Locate every malaria parasite and every leukocyte.
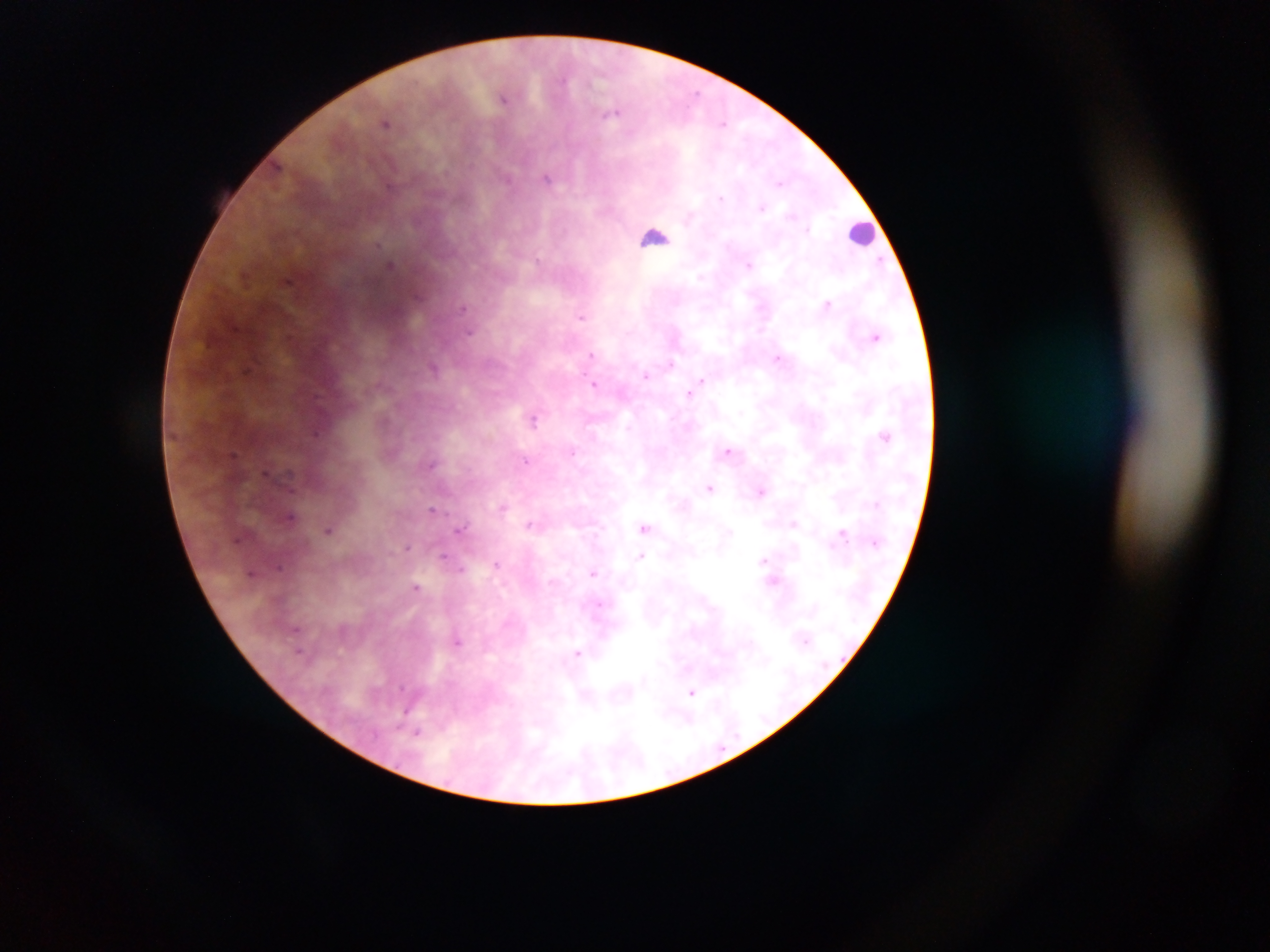
Approximate centers as {x, y} in pixels.
Malaria parasites: {504, 97}, {615, 112}, {386, 122}, {548, 177}, {751, 263}, {391, 264}, {289, 281}, {829, 303}, {582, 317}, {876, 336}, {592, 355}, {779, 358}, {670, 363}, {435, 367}, {647, 376}, {701, 380}, {595, 383}, {689, 393}, {534, 417}, {885, 435}, {728, 450}, {233, 455}, {527, 461}, {432, 462}, {266, 472}, {711, 488}, {761, 490}, {502, 507}, {432, 510}, {291, 517}, {531, 524}, {646, 527}, {462, 528}, {330, 529}, {842, 533}, {407, 548}, {445, 556}, {641, 556}, {766, 560}, {497, 563}, {253, 573}, {592, 573}, {773, 579}, {417, 587}, {599, 606}, {458, 641}, {299, 650}, {578, 654}, {693, 692}, {417, 732}.
Leukocytes: {859, 232}, {655, 237}.

Thick blood smear. Sample from Ghana. Image is 1270×952 pixels. One field of view. Mobile-phone photograph taken through the microscope.